Report the malaria status of this cell.
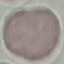
It is uninfected.

Automatically extracted cell patch, resized to 64 × 64 pixels. Acquired by smartphone through the microscope eyepiece. Giemsa stain. Thin blood smear.